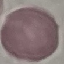 Result: no malaria parasites detected. Giemsa-stained preparation. Thin smear of blood. Automatically extracted cell patch, resized to 64 × 64 pixels. Photographed with a smartphone camera at the microscope eyepiece.